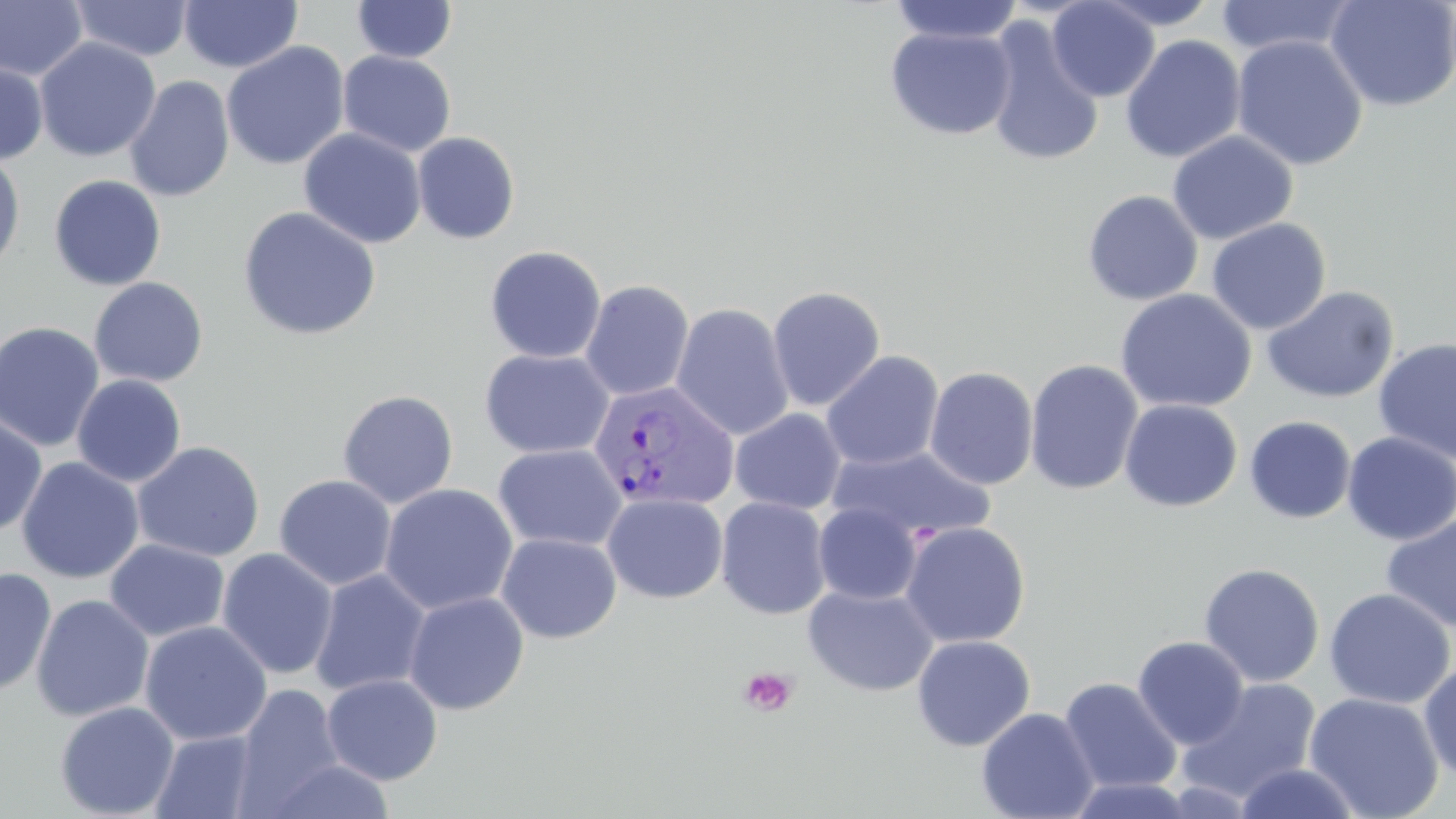
Summary:
  - Coordinate format: approximate bounding boxes as named x1/y1/x2/y2 corners in pixels
  - Platelet locations: (x1=738, y1=666, x2=799, y2=718)
  - Uninfected red blood cell locations: (x1=178, y1=0, x2=303, y2=73), (x1=352, y1=0, x2=458, y2=63), (x1=888, y1=0, x2=1024, y2=45), (x1=1046, y1=0, x2=1160, y2=102), (x1=1092, y1=0, x2=1222, y2=30), (x1=1214, y1=0, x2=1358, y2=58), (x1=1325, y1=0, x2=1456, y2=112), (x1=0, y1=1, x2=88, y2=81), (x1=69, y1=1, x2=193, y2=61), (x1=983, y1=16, x2=1105, y2=168), (x1=884, y1=24, x2=1017, y2=140), (x1=1120, y1=34, x2=1247, y2=163), (x1=1231, y1=34, x2=1369, y2=171), (x1=34, y1=38, x2=161, y2=162), (x1=221, y1=41, x2=350, y2=170), (x1=338, y1=50, x2=457, y2=157), (x1=0, y1=58, x2=49, y2=166), (x1=123, y1=75, x2=235, y2=202), (x1=298, y1=128, x2=427, y2=249), (x1=1166, y1=130, x2=1299, y2=245), (x1=413, y1=132, x2=520, y2=244), (x1=0, y1=150, x2=26, y2=275), (x1=48, y1=175, x2=167, y2=291), (x1=1082, y1=189, x2=1203, y2=305), (x1=237, y1=206, x2=382, y2=341), (x1=1206, y1=218, x2=1331, y2=335), (x1=484, y1=245, x2=606, y2=364), (x1=89, y1=277, x2=208, y2=388), (x1=580, y1=279, x2=695, y2=401), (x1=767, y1=285, x2=886, y2=412), (x1=1261, y1=285, x2=1399, y2=404), (x1=1114, y1=289, x2=1256, y2=413), (x1=670, y1=302, x2=794, y2=440), (x1=0, y1=321, x2=105, y2=452), (x1=1372, y1=338, x2=1456, y2=464), (x1=479, y1=348, x2=614, y2=460), (x1=821, y1=350, x2=944, y2=471), (x1=1025, y1=359, x2=1143, y2=495), (x1=925, y1=366, x2=1038, y2=490), (x1=72, y1=374, x2=186, y2=488), (x1=337, y1=389, x2=458, y2=509), (x1=1120, y1=399, x2=1242, y2=512), (x1=730, y1=408, x2=846, y2=514), (x1=0, y1=414, x2=48, y2=534), (x1=1244, y1=416, x2=1356, y2=523), (x1=1342, y1=432, x2=1456, y2=545), (x1=132, y1=441, x2=265, y2=562), (x1=493, y1=443, x2=627, y2=552), (x1=830, y1=446, x2=996, y2=544), (x1=16, y1=456, x2=144, y2=584), (x1=274, y1=474, x2=397, y2=591), (x1=379, y1=483, x2=518, y2=615), (x1=602, y1=493, x2=728, y2=604), (x1=715, y1=496, x2=832, y2=620), (x1=813, y1=503, x2=922, y2=605), (x1=1381, y1=513, x2=1456, y2=634), (x1=899, y1=521, x2=1031, y2=648), (x1=496, y1=533, x2=622, y2=644), (x1=105, y1=539, x2=230, y2=642), (x1=216, y1=547, x2=338, y2=680), (x1=1199, y1=562, x2=1325, y2=687), (x1=0, y1=567, x2=57, y2=696), (x1=310, y1=569, x2=431, y2=697), (x1=803, y1=584, x2=939, y2=697), (x1=1323, y1=587, x2=1455, y2=709), (x1=404, y1=591, x2=530, y2=715), (x1=30, y1=594, x2=155, y2=723), (x1=139, y1=621, x2=272, y2=746), (x1=912, y1=635, x2=1035, y2=751), (x1=1132, y1=635, x2=1249, y2=749), (x1=1419, y1=661, x2=1456, y2=780), (x1=321, y1=674, x2=443, y2=785), (x1=1059, y1=677, x2=1182, y2=794), (x1=1177, y1=679, x2=1322, y2=803), (x1=232, y1=684, x2=346, y2=814), (x1=1304, y1=692, x2=1444, y2=818), (x1=54, y1=701, x2=179, y2=818), (x1=976, y1=707, x2=1100, y2=819), (x1=150, y1=730, x2=261, y2=819), (x1=263, y1=758, x2=396, y2=818), (x1=1233, y1=761, x2=1364, y2=819), (x1=1063, y1=777, x2=1201, y2=818)
  - Plasmodium vivax-infected red blood cell locations: (x1=588, y1=380, x2=740, y2=512)
  - Slide-level diagnosis: Plasmodium vivax
  - Image size: 1456×819 pixels
  - Field of view: single
  - Modality: optical microscopy
  - Magnification: 1000x
  - Preparation: thin blood film
  - Stain: May-Grünwald-Giemsa